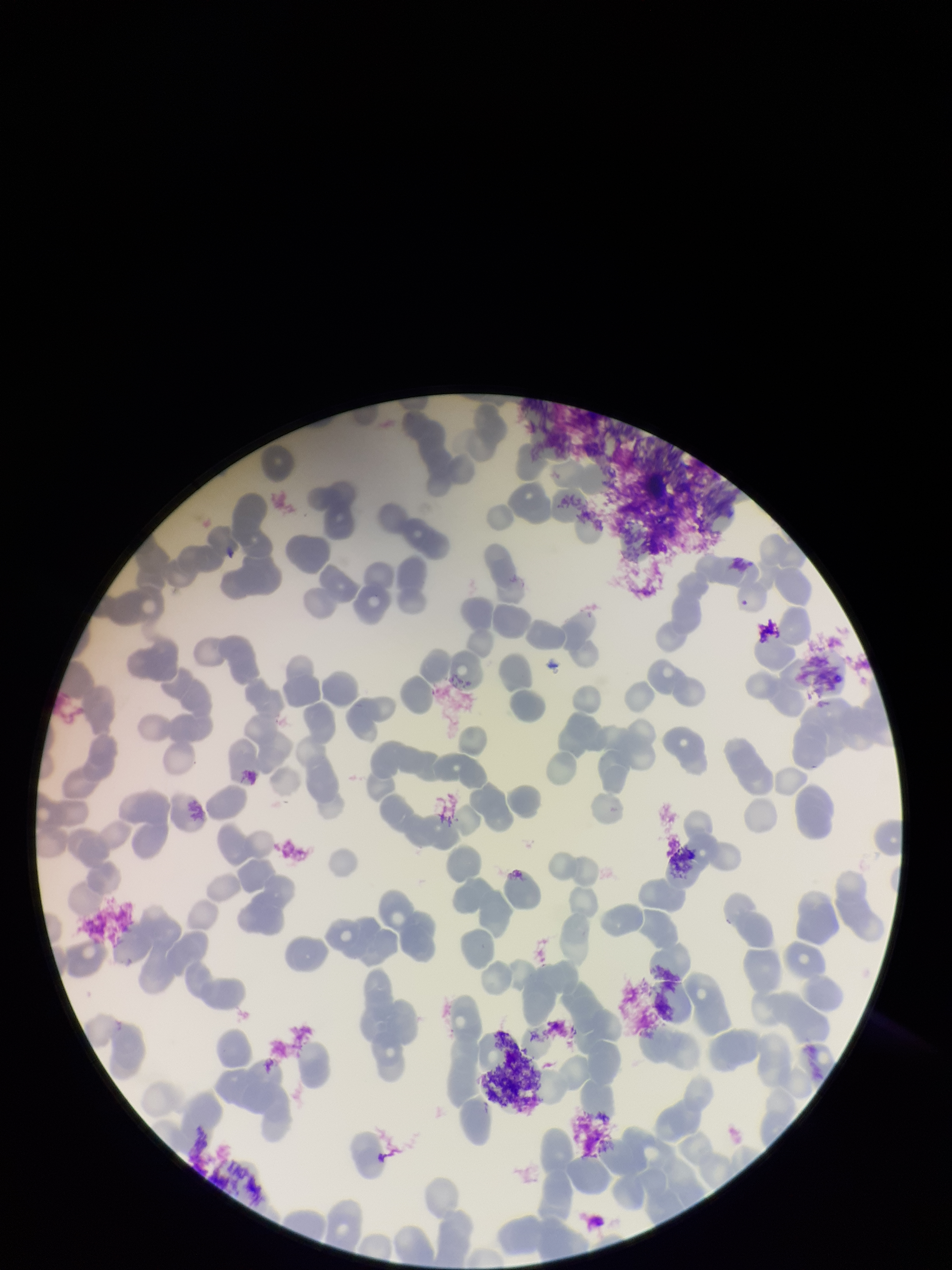
{
  "parasitized_red_blood_cell_count": 0,
  "capture": "smartphone photograph through the microscope eyepiece",
  "image_size": "952×1270 pixels",
  "species_reported_for_this_patient": "Plasmodium falciparum",
  "parasitized_red_blood_cells": "none identified",
  "red_blood_cell_count": 167,
  "field_of_view": "one from this slide",
  "patient_malaria_status": "positive",
  "stain": "Giemsa",
  "preparation": "thin smear"
}